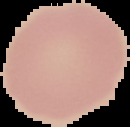

Image is 130×127 pixels. Segmented cell region on a black background. From a thin blood film. Malaria status: uninfected.